State which parasite is depicted.
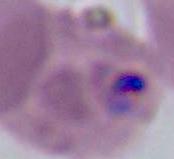
This is Plasmodium.

magnification: 400x or 1000x
modality: photomicrograph